State which cell type is depicted.
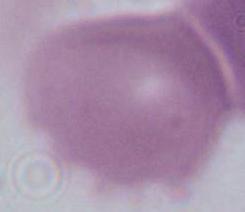
This is an erythrocyte.

magnification = 1000x
modality = micrograph